Outline each blood parasite and name the species.
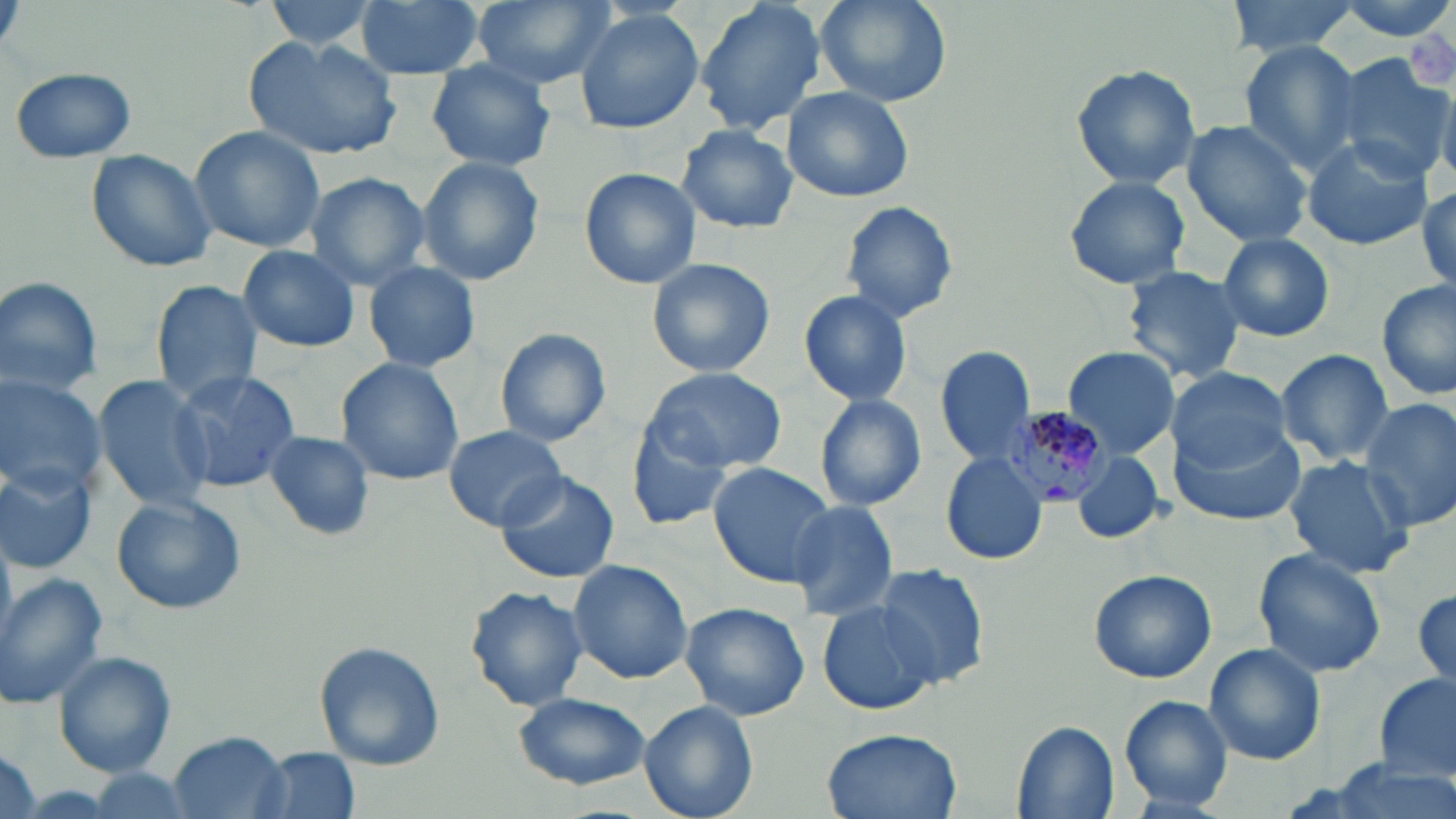

Approximate bounding boxes as (x1, y1, x2, y2) in pixels.
Plasmodium malariae-infected red blood cells: (997, 407, 1112, 508).
No Plasmodium falciparum, Plasmodium ovale, Plasmodium vivax, Babesia divergens, or Trypanosoma brucei observed.

slide-level diagnosis = Plasmodium malariae
magnification = 1000x
platelet locations = approximate bounding boxes as (x1, y1, x2, y2) in pixels: (1406, 23, 1455, 90)
field of view = single
uninfected red blood cell locations = approximate bounding boxes as (x1, y1, x2, y2) in pixels: (259, 0, 386, 53), (354, 0, 485, 79), (468, 0, 618, 90), (695, 0, 829, 136), (813, 0, 951, 108), (1225, 0, 1360, 58), (1333, 0, 1456, 43), (574, 8, 704, 135), (244, 35, 399, 160), (1238, 41, 1362, 173), (1330, 54, 1453, 178), (425, 59, 557, 170), (1068, 64, 1201, 190), (8, 66, 138, 162), (782, 86, 914, 204), (1181, 119, 1314, 246), (676, 124, 798, 234), (187, 126, 328, 256), (1303, 136, 1433, 250), (85, 149, 218, 273), (416, 157, 546, 286), (580, 168, 700, 288), (304, 171, 431, 290), (1062, 175, 1192, 289), (1416, 186, 1455, 292), (840, 200, 958, 323), (1218, 232, 1335, 343), (237, 245, 362, 353), (647, 257, 775, 379), (363, 262, 480, 373), (1121, 265, 1247, 386), (0, 276, 103, 397), (151, 279, 261, 402), (1379, 280, 1456, 402), (798, 288, 914, 407), (496, 327, 614, 446), (935, 346, 1038, 467), (1063, 347, 1178, 460), (1274, 349, 1393, 465), (335, 357, 465, 486), (642, 367, 787, 472), (1167, 368, 1291, 472), (171, 370, 299, 494), (0, 374, 106, 497), (94, 374, 216, 511), (813, 393, 928, 512), (1359, 398, 1456, 534), (623, 418, 735, 530), (1172, 423, 1309, 526), (442, 426, 568, 531), (263, 430, 374, 540), (1070, 449, 1163, 544), (940, 452, 1049, 566), (1284, 455, 1416, 579), (0, 461, 99, 574), (707, 462, 837, 586), (493, 469, 619, 583), (111, 493, 245, 615), (784, 500, 901, 621), (1252, 547, 1387, 680), (567, 559, 695, 684), (872, 563, 989, 688), (1087, 569, 1217, 684), (0, 573, 106, 706), (465, 585, 590, 712), (1412, 585, 1456, 690), (817, 597, 946, 717), (679, 602, 809, 721), (313, 641, 445, 770), (1204, 643, 1326, 765), (57, 651, 177, 775), (1376, 674, 1455, 781), (512, 693, 652, 792), (1120, 695, 1234, 810), (640, 701, 759, 819), (1010, 719, 1120, 819), (821, 728, 962, 819), (170, 731, 288, 817), (2, 747, 43, 819), (256, 748, 360, 819), (1318, 761, 1452, 819)
stain = May-Grünwald-Giemsa
preparation = thin blood film
modality = light microscopy
image size = 1456×819 pixels